Comment on the morphology of the red blood cells.
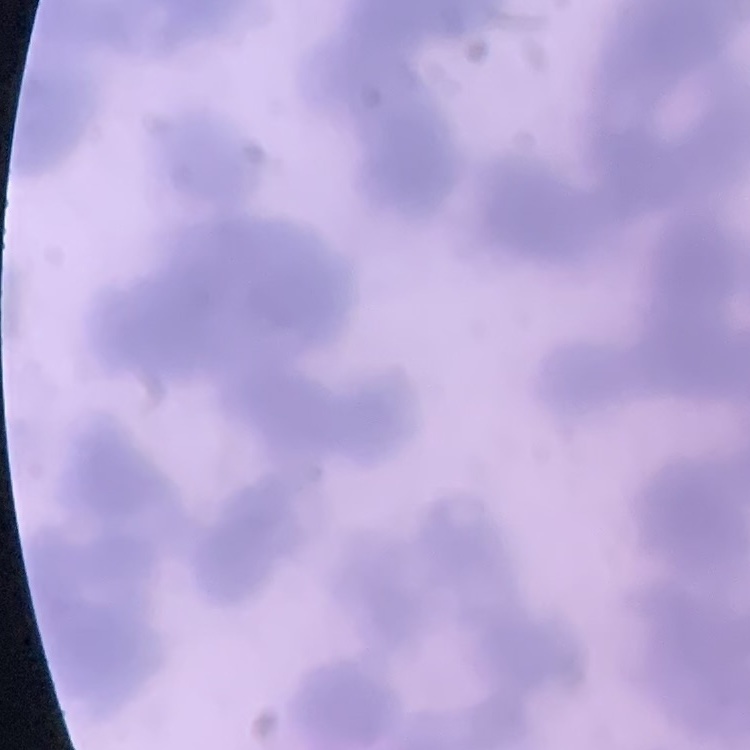
They show rouleaux formation.

Thin peripheral smear. One tile cut from a larger photomicrograph. Stained with either Field's or Giemsa.